Outline each uninfected red blood cell.
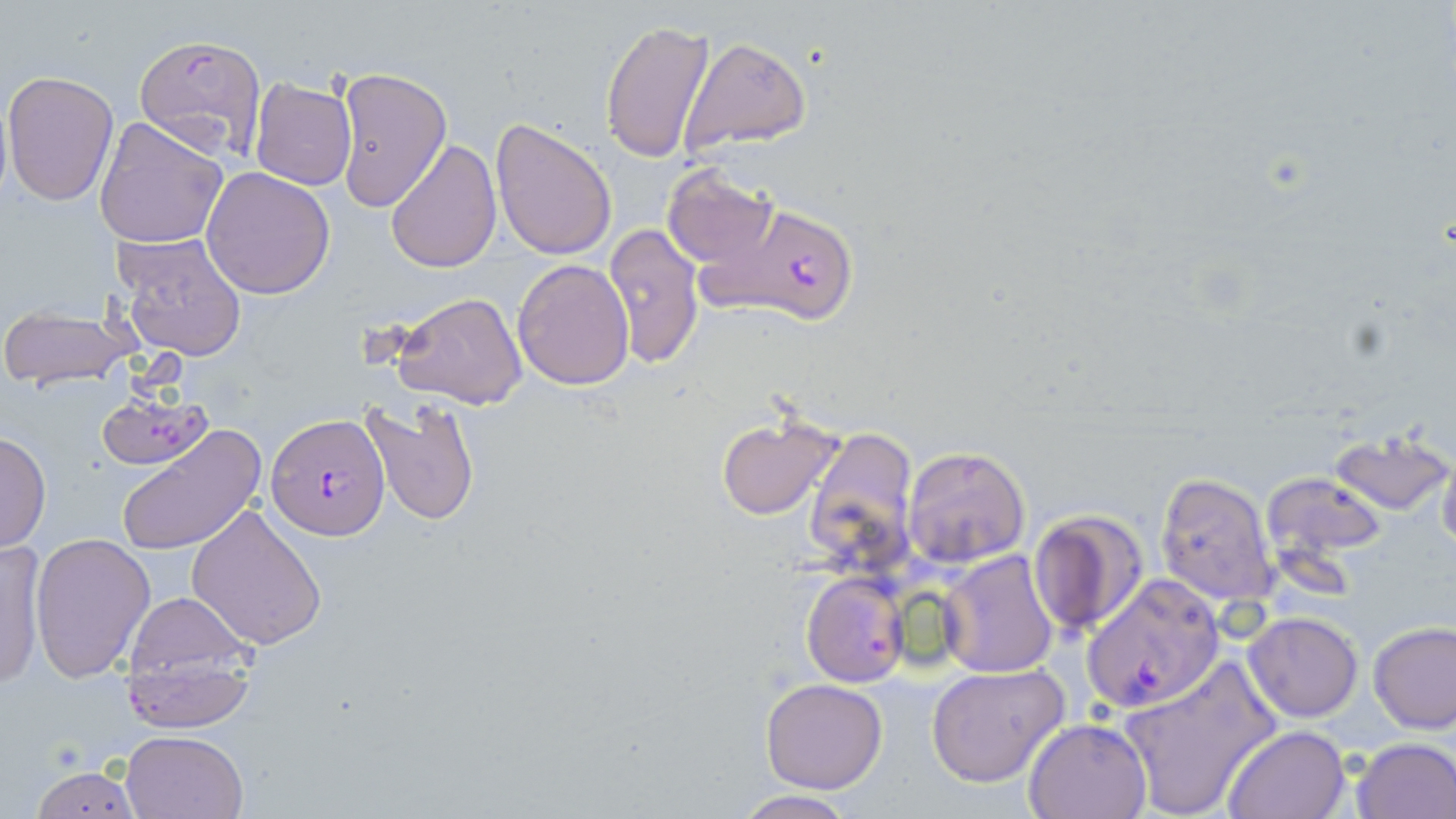
Approximate bounding boxes as (x1,y1)-(x2,y2) corner pairs in pixels.
Uninfected red blood cells: (599,17)-(715,166), (680,36)-(812,154), (332,67)-(450,213), (1,71)-(120,208), (250,78)-(356,190), (93,116)-(227,250), (490,117)-(618,261), (385,138)-(502,272), (662,163)-(777,275), (202,167)-(335,299), (603,222)-(706,371), (112,232)-(249,361), (512,258)-(636,391), (392,290)-(529,411), (0,304)-(141,391), (362,396)-(481,526), (714,411)-(843,520), (116,423)-(264,555), (803,425)-(921,582), (1327,428)-(1454,516), (0,430)-(50,553), (904,446)-(1031,568), (1438,447)-(1456,558), (1261,472)-(1389,566), (1156,473)-(1280,607), (186,502)-(328,651), (1028,510)-(1149,638), (29,532)-(155,682), (0,540)-(47,690), (938,551)-(1059,678), (802,572)-(908,686), (116,588)-(262,713), (1244,612)-(1363,723), (1368,619)-(1456,734), (117,660)-(258,733), (1117,660)-(1279,819), (925,664)-(1068,788), (759,677)-(888,792), (1021,717)-(1151,819), (1221,723)-(1351,818), (121,729)-(248,819), (1351,737)-(1456,819), (26,762)-(145,819), (733,791)-(860,819).

Plasmodium falciparum-infected red blood cell locations: (134,32)-(268,160), (685,207)-(862,326), (267,412)-(390,539), (1082,575)-(1225,713). Slide-level diagnosis: Plasmodium falciparum. Light microscopy. 1000x magnification. Image is 1456×819 pixels. Single field of view. Thin blood film. May-Grünwald-Giemsa-stained preparation.